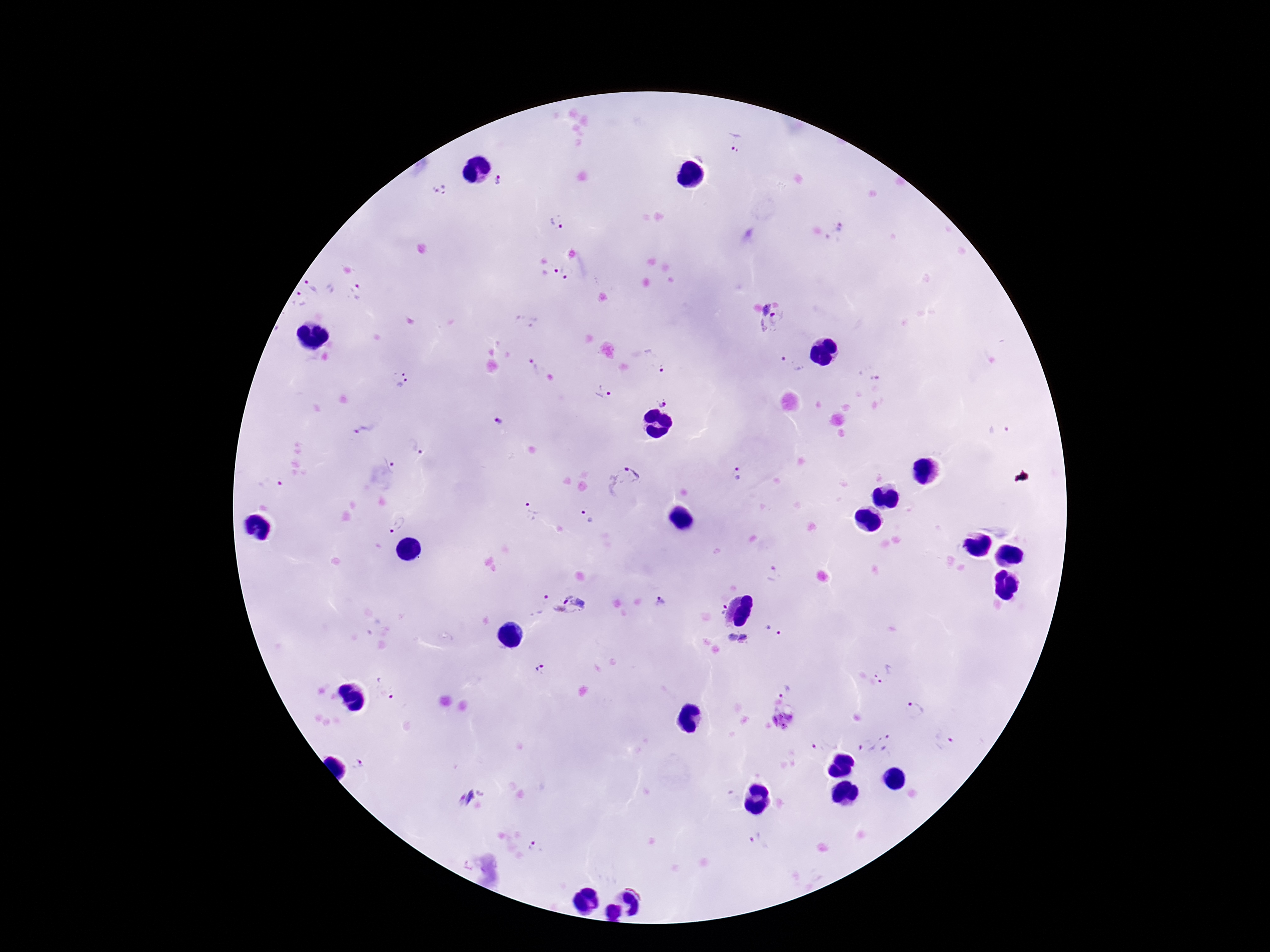
Approximate centers as {x, y} in pixels. Plasmodium parasite locations: {735, 140}, {499, 180}, {440, 189}, {558, 221}, {838, 233}, {552, 269}, {570, 275}, {312, 285}, {356, 292}, {299, 299}, {772, 320}, {658, 359}, {791, 364}, {536, 367}, {873, 369}, {400, 380}, {603, 393}, {667, 403}, {499, 422}, {1002, 430}, {369, 431}, {413, 448}, {394, 463}, {736, 473}, {622, 480}, {271, 483}, {531, 512}, {587, 516}, {398, 524}, {776, 575}, {661, 599}, {536, 604}, {568, 607}, {722, 610}, {774, 629}, {745, 639}, {731, 640}, {540, 667}, {886, 671}, {385, 687}, {785, 690}, {913, 710}, {783, 721}, {944, 738}, {888, 743}, {865, 745}, {821, 746}, {357, 764}, {466, 797}, {757, 838}, {537, 848}. 100x magnification. Giemsa-stained preparation. Smartphone photograph taken through the microscope eyepiece. Image is 1270×952 pixels. Thick blood smear. Patient malaria status: positive. One field from this slide.